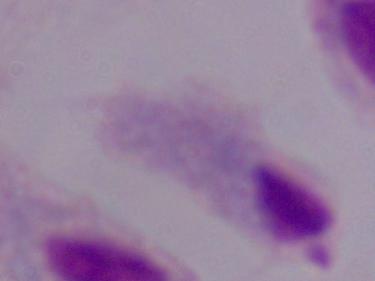
Summary:
  - Magnification: 1000x
  - Identification: trichomonad
  - Modality: photomicrograph